Assess this cell for malaria.
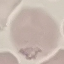

Uninfected.

{
  "capture": "smartphone through the microscope eyepiece",
  "preparation": "thin blood smear",
  "image_type": "cell patch, automatically extracted from a larger field of view and resized to 64 × 64 pixels",
  "stain": "Giemsa"
}